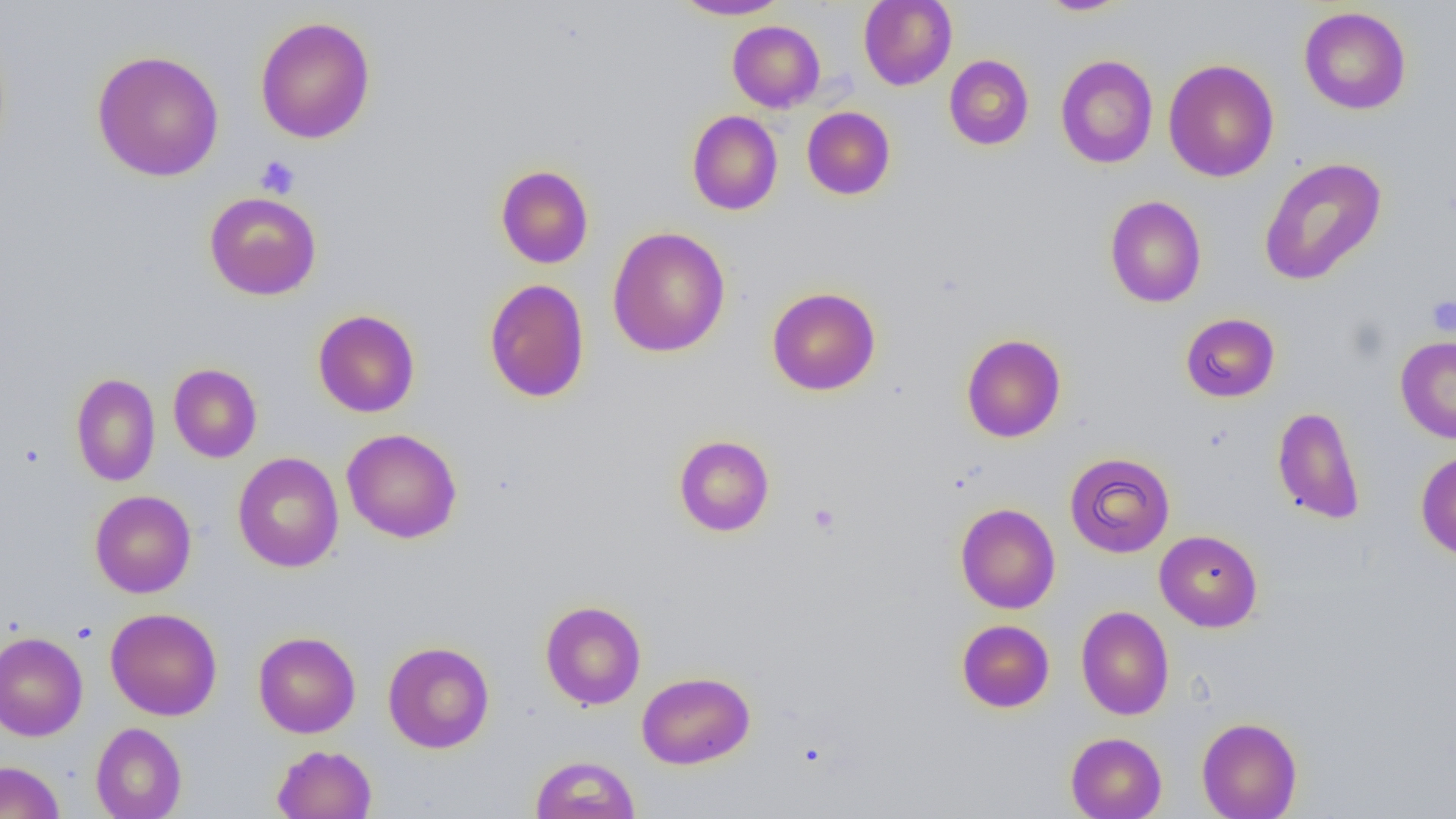
slide-level diagnosis = no evidence of blood parasites
magnification = 1000x
image size = 1456×819 pixels
preparation = thin blood smear
platelet locations = approximate bounding boxes as [x1, y1, x2, y2] in pixels: [255, 155, 301, 198], [1426, 295, 1456, 336], [808, 503, 840, 534]
field of view = one of a larger specimen
modality = optical microscopy
uninfected red blood cell locations = approximate bounding boxes as [x1, y1, x2, y2] in pixels: [674, 0, 789, 19], [858, 0, 957, 90], [1036, 0, 1135, 16], [1298, 6, 1411, 114], [255, 16, 375, 144], [727, 20, 825, 112], [92, 50, 225, 182], [1056, 54, 1158, 169], [944, 55, 1034, 150], [1163, 59, 1279, 182], [802, 107, 895, 199], [686, 110, 783, 215], [1258, 157, 1387, 286], [495, 164, 594, 269], [204, 192, 322, 300], [1105, 195, 1207, 308], [607, 226, 731, 358], [483, 278, 591, 403], [767, 287, 881, 396], [313, 309, 420, 417], [1180, 313, 1280, 402], [961, 334, 1066, 442], [1395, 337, 1456, 443], [168, 363, 262, 463], [70, 373, 160, 486], [1272, 405, 1365, 524], [341, 428, 463, 543], [673, 434, 774, 537], [1415, 449, 1456, 560], [232, 452, 344, 572], [1064, 452, 1175, 558], [89, 490, 197, 598], [955, 503, 1060, 613], [1154, 530, 1263, 631], [540, 600, 646, 710], [1075, 606, 1174, 720], [105, 607, 223, 720], [956, 617, 1173, 711], [956, 619, 1054, 712], [253, 631, 361, 738], [0, 632, 88, 742], [382, 641, 495, 753], [636, 671, 755, 769], [1196, 716, 1303, 818], [90, 722, 186, 819], [1066, 732, 1167, 819], [272, 744, 377, 818], [529, 754, 641, 818], [0, 760, 65, 819]